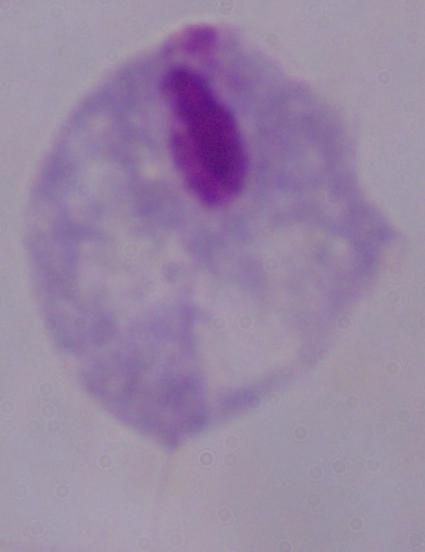
A trichomonad is seen. Micrograph. Captured at 1000x magnification.